Locate every blood parasite and identify its species.
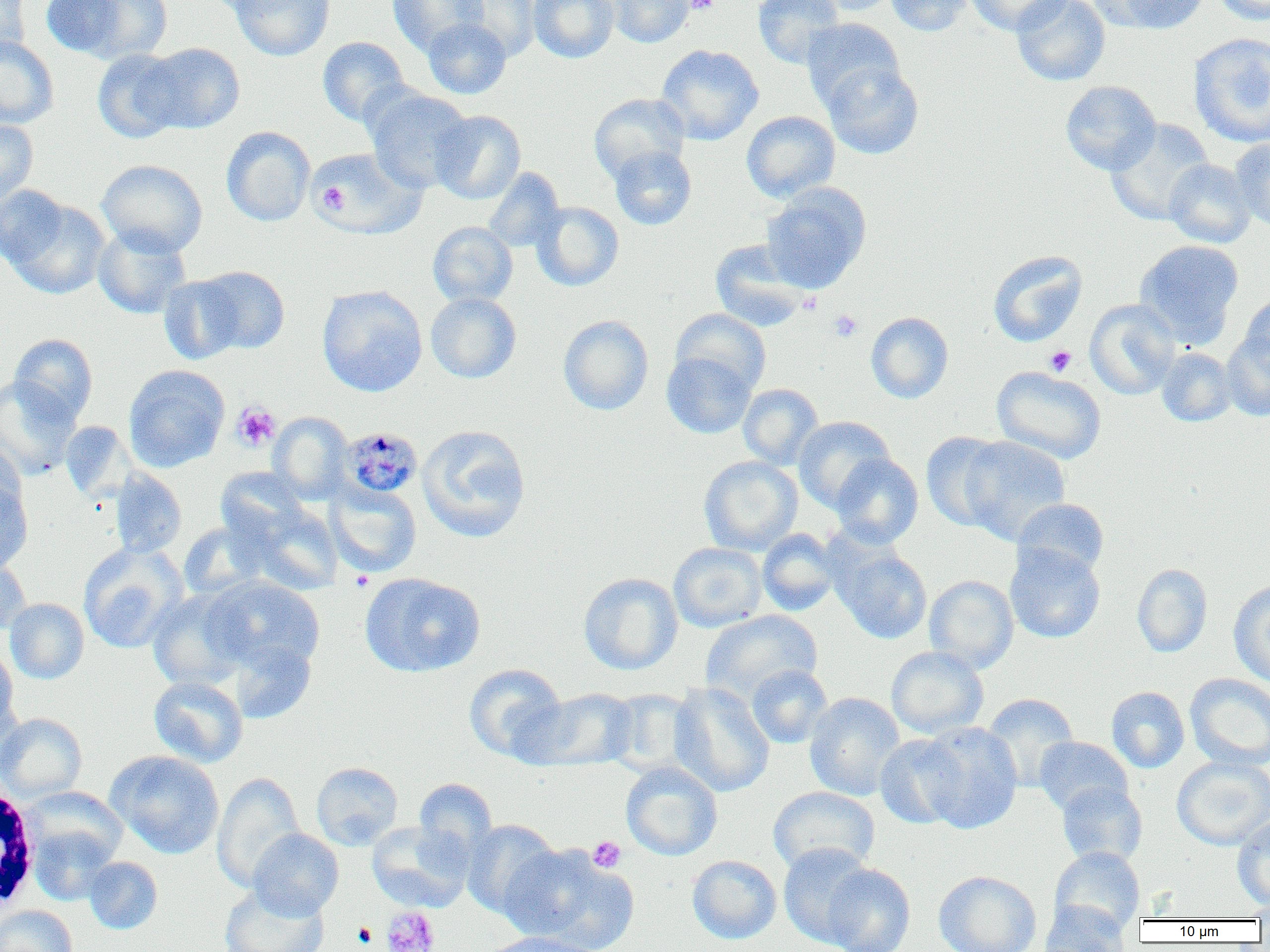

Approximate bounding boxes as (x1,y1)-(x2,y2) corner pairs in pixels.
Plasmodium malariae-infected red blood cells: (339,427)-(423,500).
No Plasmodium falciparum, Plasmodium ovale, Plasmodium vivax, Babesia divergens, or Trypanosoma brucei observed.

White blood cell locations: (0,777)-(42,917). Platelet locations: (684,0)-(719,14), (314,169)-(365,220), (317,182)-(349,214), (799,292)-(821,314), (828,310)-(863,342), (1044,346)-(1077,377), (231,403)-(280,451), (349,571)-(373,592), (588,836)-(626,873), (381,906)-(440,952), (351,922)-(378,948). Uninfected red blood cell locations: (0,0)-(31,62), (203,0)-(290,16), (229,0)-(335,61), (387,0)-(486,54), (529,0)-(619,63), (606,0)-(694,48), (753,0)-(844,69), (806,0)-(898,15), (884,0)-(975,36), (965,0)-(1072,36), (1011,0)-(1110,86), (1096,0)-(1211,34), (1213,0)-(1270,25), (61,1)-(173,63), (453,1)-(540,61), (422,18)-(512,99), (801,18)-(904,111), (1188,33)-(1270,148), (0,36)-(59,129), (317,36)-(409,126), (138,42)-(245,134), (656,44)-(764,145), (92,49)-(187,143), (822,60)-(924,159), (1060,80)-(1161,175), (365,88)-(473,193), (589,93)-(689,183), (430,110)-(526,204), (741,111)-(840,202), (0,119)-(38,204), (1105,119)-(1214,226), (221,126)-(315,226), (1231,138)-(1270,231), (609,146)-(697,230), (310,147)-(426,238), (97,159)-(207,256), (1163,159)-(1256,248), (482,167)-(565,252), (761,183)-(871,292), (0,184)-(70,268), (4,196)-(111,300), (531,201)-(624,291), (427,221)-(518,308), (93,225)-(191,319), (710,239)-(810,331), (1134,239)-(1244,345), (987,250)-(1087,347), (196,266)-(290,355), (158,274)-(247,365), (317,285)-(427,397), (425,292)-(522,383), (1239,293)-(1270,374), (1084,299)-(1180,399), (671,308)-(771,396), (866,312)-(954,403), (558,314)-(654,415), (1221,331)-(1270,421), (9,333)-(98,423), (1156,347)-(1236,426), (662,352)-(756,439), (123,365)-(229,472), (991,366)-(1107,463), (0,376)-(81,481), (737,383)-(823,469), (268,411)-(353,503), (793,416)-(895,511), (60,421)-(135,503), (417,424)-(531,543), (921,431)-(1013,531), (958,435)-(1071,544), (0,442)-(27,521), (831,447)-(1014,538), (830,453)-(923,548), (699,456)-(803,555), (216,466)-(310,544), (110,469)-(187,559), (0,478)-(33,574), (325,482)-(421,577), (1013,498)-(1110,579), (245,502)-(343,594), (178,521)-(267,600), (757,528)-(844,616), (668,542)-(767,632), (78,543)-(187,653), (832,544)-(932,644), (1005,544)-(1105,644), (0,553)-(31,636), (1132,563)-(1213,657), (360,572)-(485,678), (578,572)-(683,675), (924,575)-(1019,674), (203,576)-(325,673), (1228,580)-(1270,686), (147,588)-(252,690), (5,598)-(89,684), (701,609)-(823,705), (229,639)-(316,724), (0,644)-(18,737), (886,646)-(989,738), (464,663)-(568,762), (746,664)-(833,748), (1185,673)-(1270,771), (148,675)-(248,767), (669,682)-(774,797), (522,687)-(639,772), (1106,687)-(1189,773), (604,688)-(700,777), (804,692)-(905,801), (982,693)-(1080,790), (0,713)-(87,801), (916,721)-(1023,833), (875,734)-(968,829), (1034,736)-(1132,816), (106,750)-(225,858), (1172,756)-(1270,850), (311,761)-(403,850), (620,761)-(722,861), (211,772)-(305,892), (414,778)-(497,857), (1056,781)-(1148,868), (19,786)-(128,872), (768,786)-(880,875), (1232,815)-(1270,910), (462,819)-(561,918), (367,820)-(474,912), (26,824)-(119,906), (248,828)-(343,919), (778,842)-(877,947), (500,844)-(638,951), (1049,846)-(1145,937), (687,855)-(782,943), (83,857)-(162,934), (821,863)-(915,952), (933,870)-(1042,952), (218,883)-(329,952), (1038,901)-(1130,952), (1242,901)-(1270,920), (0,905)-(78,952), (479,932)-(603,952). Slide-level diagnosis: Plasmodium malariae. Thin blood smear. Optical microscopy. 1000x magnification. Single field of view. Image is 1270×952 pixels.